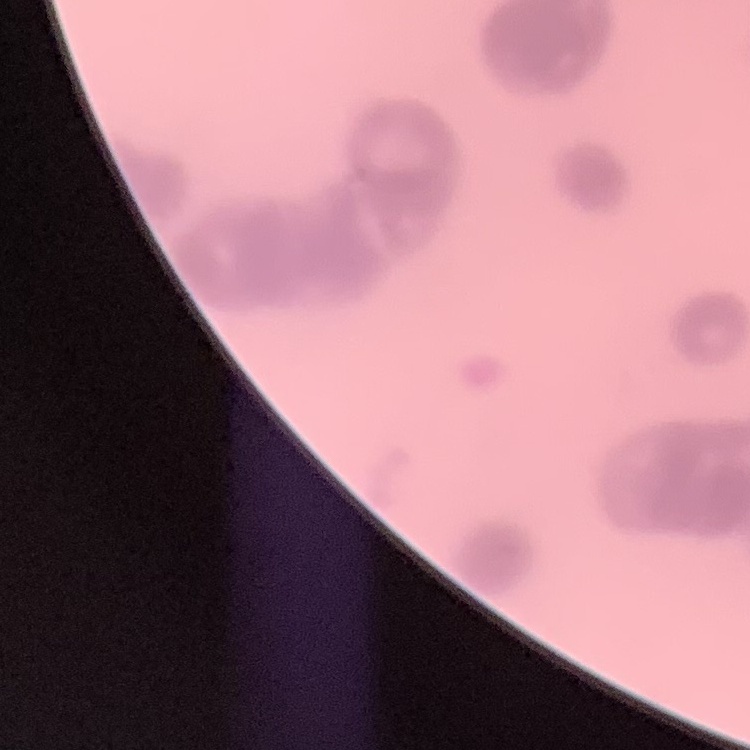 The erythrocytes exhibit rouleaux formation. Thin blood smear. Square crop of a larger photomicrograph. Stained with either Field's or Giemsa.